Name the cell type shown.
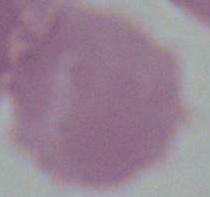

An erythrocyte.

Captured at 1000x magnification. Photomicrograph.